Name the blood parasite species.
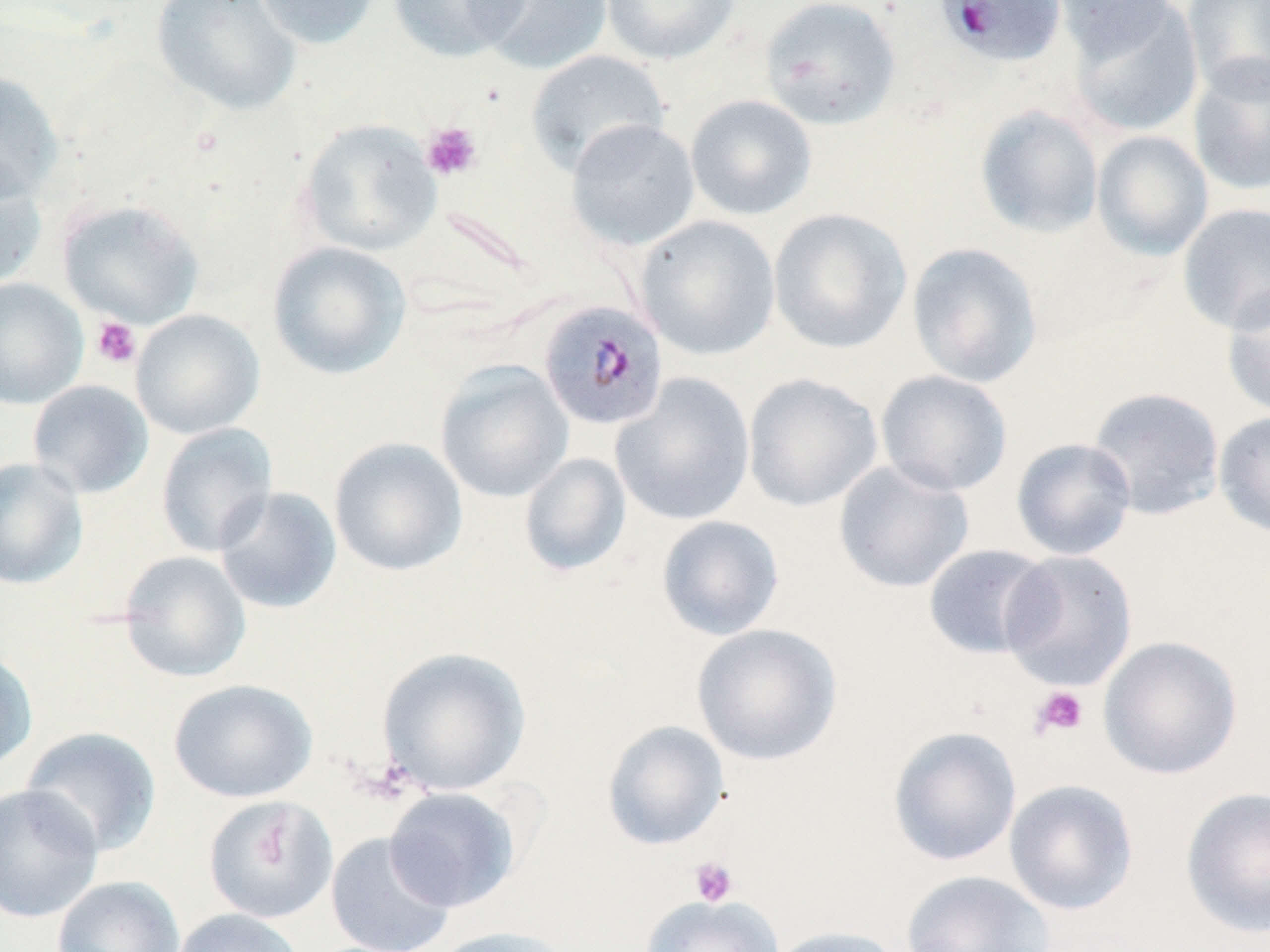

Plasmodium malariae.

modality = optical microscopy
platelet locations = approximate bounding boxes as named x1/y1/x2/y2 corners in pixels: (x1=421, y1=122, x2=483, y2=181), (x1=91, y1=316, x2=142, y2=368), (x1=1030, y1=686, x2=1089, y2=738), (x1=689, y1=856, x2=739, y2=907)
magnification = 1000x
field of view = single
stain = May-Grünwald-Giemsa
image size = 1270×952 pixels
uninfected red blood cell locations = approximate bounding boxes as named x1/y1/x2/y2 corners in pixels: (x1=150, y1=0, x2=301, y2=116), (x1=252, y1=0, x2=381, y2=50), (x1=388, y1=0, x2=530, y2=62), (x1=474, y1=0, x2=614, y2=75), (x1=600, y1=0, x2=741, y2=65), (x1=760, y1=0, x2=902, y2=130), (x1=1050, y1=0, x2=1181, y2=58), (x1=1182, y1=0, x2=1270, y2=99), (x1=1067, y1=1, x2=1204, y2=138), (x1=525, y1=49, x2=670, y2=177), (x1=1187, y1=56, x2=1270, y2=197), (x1=0, y1=70, x2=64, y2=205), (x1=685, y1=94, x2=817, y2=221), (x1=974, y1=105, x2=1104, y2=239), (x1=298, y1=118, x2=441, y2=256), (x1=565, y1=118, x2=700, y2=251), (x1=1091, y1=130, x2=1214, y2=260), (x1=0, y1=156, x2=47, y2=292), (x1=58, y1=199, x2=205, y2=328), (x1=1176, y1=202, x2=1270, y2=334), (x1=768, y1=207, x2=913, y2=354), (x1=635, y1=215, x2=781, y2=360), (x1=267, y1=241, x2=412, y2=380), (x1=906, y1=242, x2=1043, y2=388), (x1=0, y1=277, x2=88, y2=409), (x1=1221, y1=283, x2=1270, y2=419), (x1=131, y1=309, x2=265, y2=439), (x1=434, y1=360, x2=574, y2=503), (x1=875, y1=369, x2=1013, y2=497), (x1=610, y1=373, x2=756, y2=526), (x1=742, y1=373, x2=882, y2=511), (x1=27, y1=380, x2=154, y2=499), (x1=1086, y1=386, x2=1226, y2=521), (x1=1213, y1=411, x2=1270, y2=539), (x1=156, y1=422, x2=277, y2=557), (x1=329, y1=437, x2=468, y2=576), (x1=1011, y1=437, x2=1137, y2=561), (x1=519, y1=452, x2=631, y2=576), (x1=0, y1=457, x2=88, y2=590), (x1=833, y1=459, x2=974, y2=594), (x1=214, y1=486, x2=342, y2=615), (x1=656, y1=515, x2=785, y2=641), (x1=922, y1=544, x2=1055, y2=659), (x1=999, y1=549, x2=1138, y2=691), (x1=117, y1=550, x2=251, y2=682), (x1=692, y1=622, x2=842, y2=766), (x1=1098, y1=635, x2=1243, y2=780), (x1=0, y1=646, x2=38, y2=775), (x1=377, y1=646, x2=531, y2=796), (x1=168, y1=678, x2=317, y2=803), (x1=602, y1=720, x2=729, y2=850), (x1=20, y1=726, x2=162, y2=858), (x1=887, y1=726, x2=1022, y2=867), (x1=1003, y1=779, x2=1139, y2=915), (x1=0, y1=783, x2=103, y2=924), (x1=1180, y1=786, x2=1270, y2=938), (x1=384, y1=787, x2=520, y2=912), (x1=203, y1=796, x2=338, y2=924), (x1=325, y1=832, x2=455, y2=952), (x1=901, y1=870, x2=1055, y2=952), (x1=51, y1=875, x2=185, y2=952), (x1=639, y1=894, x2=784, y2=952), (x1=172, y1=908, x2=304, y2=952), (x1=768, y1=925, x2=905, y2=952), (x1=431, y1=926, x2=577, y2=952)
preparation = thin blood smear
Plasmodium malariae-infected red blood cell locations = approximate bounding boxes as named x1/y1/x2/y2 corners in pixels: (x1=934, y1=0, x2=1067, y2=68), (x1=537, y1=300, x2=668, y2=431)